Give the position of every Plasmodium parasite.
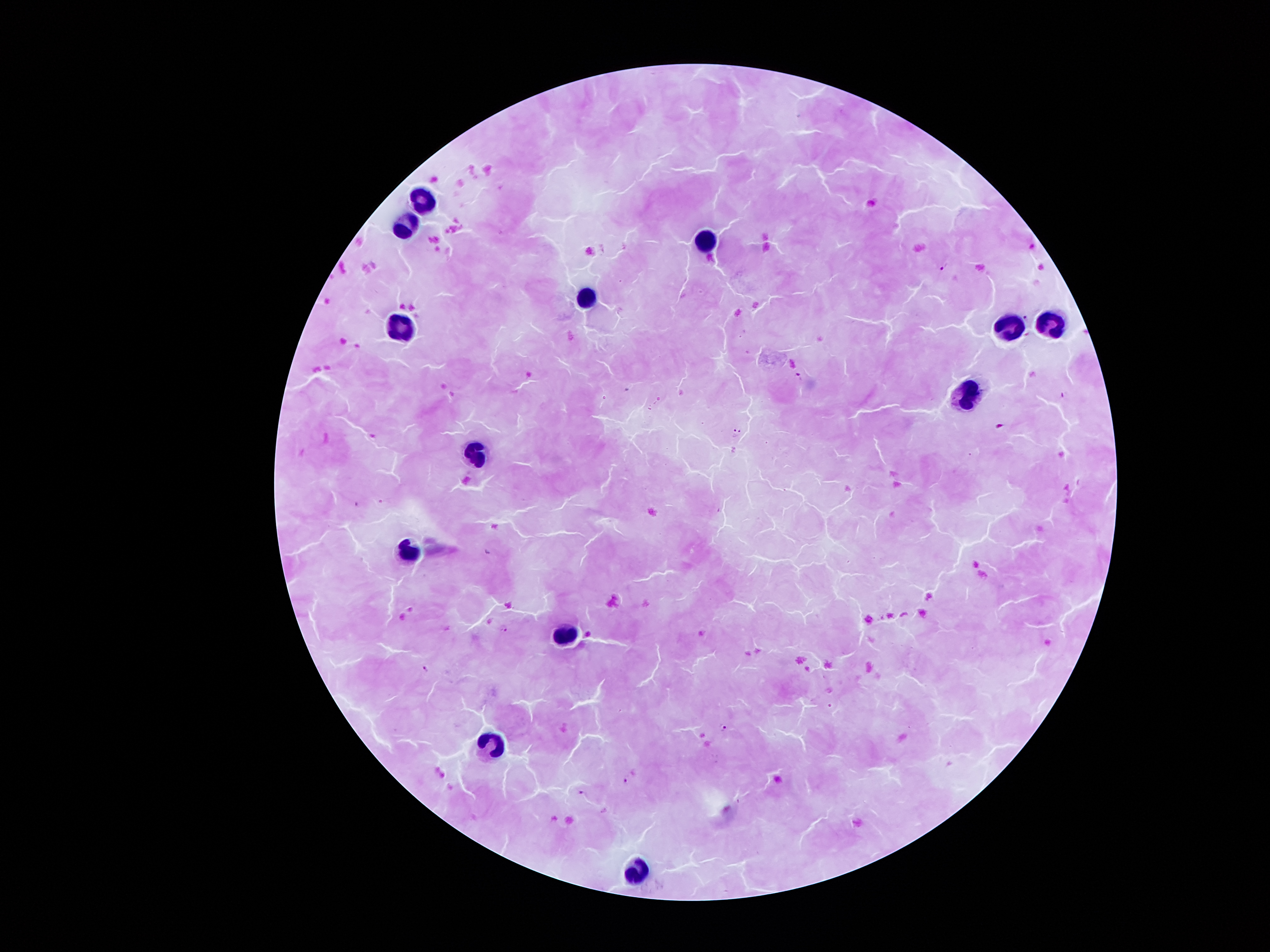
Approximate centers as (x, y) in pixels.
Plasmodium parasites: (942, 267), (1026, 317), (798, 375), (1064, 394), (1001, 425), (737, 431), (506, 628), (425, 668), (722, 727), (625, 780), (579, 792).

Leukocyte locations: (419, 197), (408, 228), (703, 241), (584, 301), (1053, 326), (399, 329), (1007, 332), (968, 400), (475, 456), (405, 550), (569, 631), (489, 746), (637, 866). Smartphone photograph taken through the microscope eyepiece. Giemsa-stained preparation. One field from this slide. 100x magnification. Patient malaria status: positive for Plasmodium falciparum. Thick peripheral-blood smear. Image is 1270×952 pixels.